State which parasite is depicted.
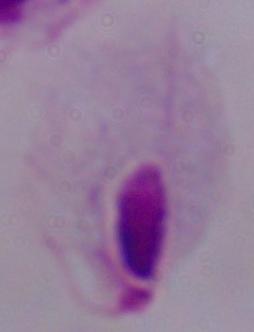

A trichomonad.

{
  "modality": "photomicrograph",
  "magnification": "1000x"
}